Comment on the morphology of the red blood cells.
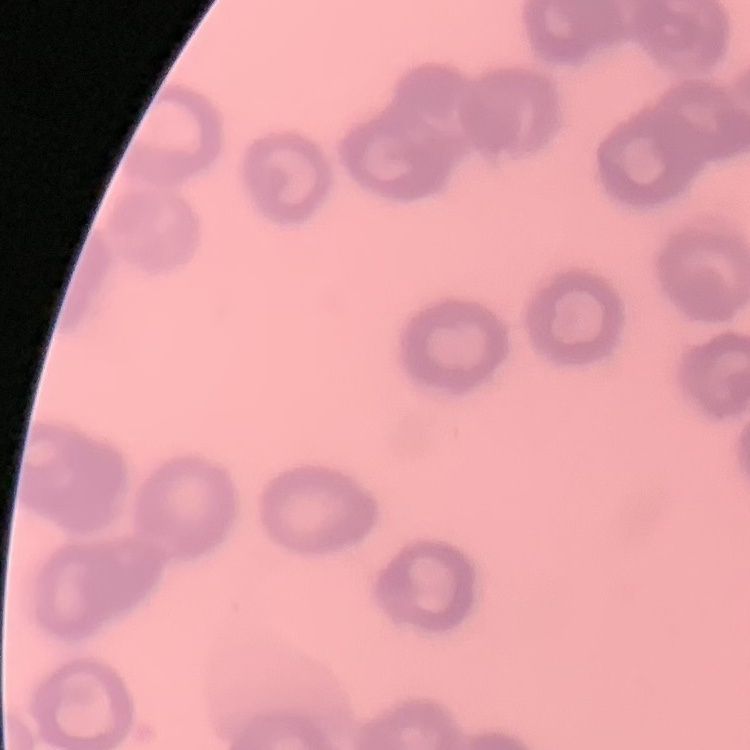
Rouleaux formation.

Square crop of a larger photomicrograph. Stained with either Field's or Giemsa. Thin blood film.